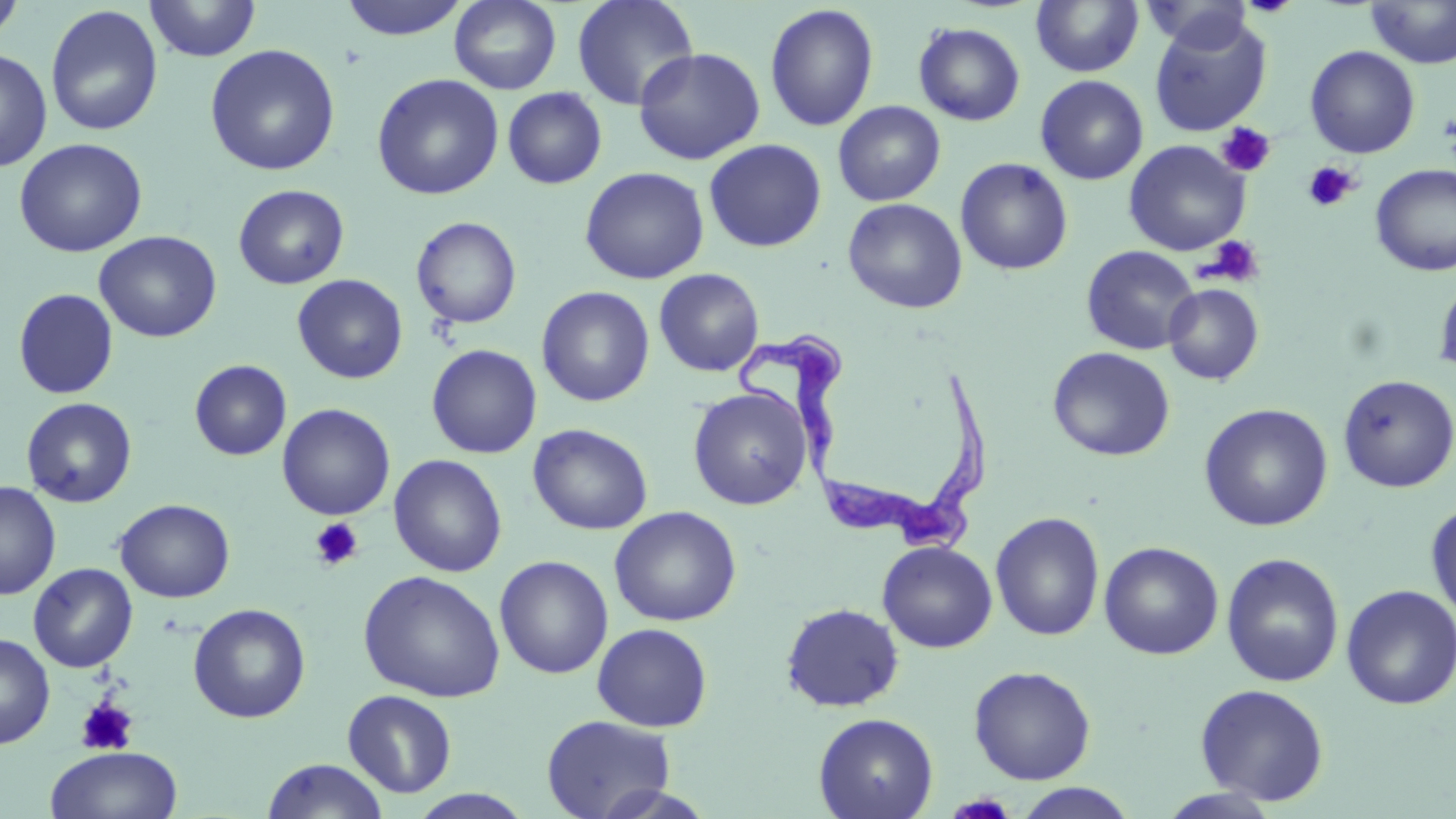

Approximate bounding boxes as named x1/y1/x2/y2 corners in pixels. Trypanosoma brucei locations: (x1=740, y1=335, x2=987, y2=558). Platelet locations: (x1=1438, y1=113, x2=1455, y2=147), (x1=1216, y1=122, x2=1276, y2=177), (x1=1302, y1=162, x2=1359, y2=212), (x1=1202, y1=235, x2=1265, y2=287), (x1=309, y1=517, x2=363, y2=572), (x1=75, y1=697, x2=139, y2=756). Uninfected red blood cell locations: (x1=0, y1=0, x2=25, y2=47), (x1=143, y1=0, x2=261, y2=61), (x1=338, y1=0, x2=471, y2=41), (x1=449, y1=0, x2=562, y2=94), (x1=572, y1=0, x2=699, y2=111), (x1=1031, y1=0, x2=1144, y2=77), (x1=1145, y1=0, x2=1256, y2=54), (x1=1238, y1=0, x2=1300, y2=17), (x1=1365, y1=1, x2=1456, y2=69), (x1=764, y1=4, x2=879, y2=132), (x1=44, y1=5, x2=164, y2=137), (x1=1149, y1=13, x2=1272, y2=137), (x1=914, y1=22, x2=1025, y2=125), (x1=204, y1=44, x2=341, y2=176), (x1=1305, y1=45, x2=1421, y2=158), (x1=633, y1=46, x2=766, y2=165), (x1=0, y1=47, x2=52, y2=172), (x1=371, y1=73, x2=504, y2=200), (x1=1035, y1=75, x2=1148, y2=185), (x1=502, y1=87, x2=607, y2=189), (x1=833, y1=100, x2=946, y2=206), (x1=14, y1=137, x2=148, y2=257), (x1=704, y1=139, x2=826, y2=252), (x1=1123, y1=140, x2=1250, y2=256), (x1=955, y1=157, x2=1073, y2=275), (x1=1370, y1=163, x2=1456, y2=278), (x1=579, y1=166, x2=709, y2=285), (x1=233, y1=184, x2=349, y2=289), (x1=843, y1=198, x2=967, y2=314), (x1=411, y1=216, x2=522, y2=329), (x1=94, y1=231, x2=222, y2=343), (x1=1081, y1=245, x2=1200, y2=355), (x1=654, y1=268, x2=764, y2=377), (x1=1434, y1=273, x2=1456, y2=379), (x1=292, y1=274, x2=408, y2=384), (x1=1164, y1=284, x2=1263, y2=385), (x1=536, y1=286, x2=655, y2=407), (x1=13, y1=288, x2=119, y2=399), (x1=426, y1=344, x2=542, y2=459), (x1=1048, y1=346, x2=1175, y2=461), (x1=189, y1=359, x2=291, y2=461), (x1=1337, y1=374, x2=1456, y2=493), (x1=688, y1=387, x2=812, y2=510), (x1=21, y1=397, x2=137, y2=508), (x1=277, y1=403, x2=395, y2=521), (x1=1199, y1=403, x2=1334, y2=531), (x1=528, y1=423, x2=652, y2=535), (x1=388, y1=454, x2=507, y2=577), (x1=0, y1=481, x2=61, y2=600), (x1=114, y1=498, x2=235, y2=603), (x1=1426, y1=498, x2=1456, y2=628), (x1=608, y1=506, x2=742, y2=626), (x1=990, y1=511, x2=1105, y2=641), (x1=877, y1=541, x2=998, y2=653), (x1=1099, y1=541, x2=1223, y2=660), (x1=1221, y1=553, x2=1345, y2=688), (x1=494, y1=555, x2=613, y2=679), (x1=28, y1=562, x2=138, y2=672), (x1=358, y1=569, x2=506, y2=703), (x1=1340, y1=585, x2=1456, y2=710), (x1=780, y1=602, x2=904, y2=712), (x1=188, y1=603, x2=311, y2=723), (x1=592, y1=623, x2=713, y2=732), (x1=0, y1=631, x2=55, y2=749), (x1=968, y1=665, x2=1097, y2=785), (x1=1194, y1=683, x2=1330, y2=805), (x1=342, y1=689, x2=457, y2=798), (x1=813, y1=712, x2=938, y2=819), (x1=541, y1=715, x2=676, y2=819), (x1=44, y1=745, x2=183, y2=819), (x1=262, y1=758, x2=389, y2=818), (x1=586, y1=783, x2=721, y2=818), (x1=1012, y1=784, x2=1139, y2=819), (x1=1155, y1=787, x2=1283, y2=818), (x1=407, y1=789, x2=535, y2=818). Slide-level diagnosis: Trypanosoma brucei. Captured at 1000x magnification. Light microscopy. May-Grünwald-Giemsa stain. Thin blood film. One field of a larger specimen. Image is 1456×819 pixels.